Assess this cell for malaria.
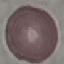

Uninfected.

Summary:
  - Capture: smartphone camera at the microscope eyepiece
  - Image type: cell patch, automatically extracted from a larger field of view and resized to 64 × 64 pixels
  - Preparation: thin blood film
  - Stain: Giemsa